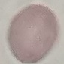
{
  "result": "no malaria parasites detected",
  "stain": "Giemsa",
  "preparation": "thin blood smear",
  "capture": "smartphone camera at the microscope eyepiece",
  "image_type": "cell patch, automatically extracted from a larger field of view and resized to 64 × 64 pixels"
}